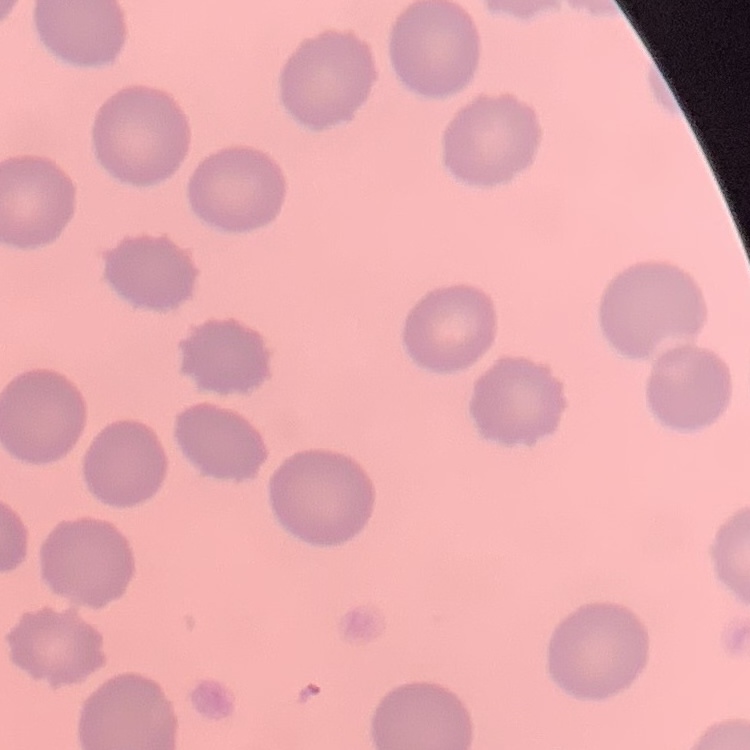
The erythrocytes show no rouleaux formation. Thin peripheral smear. Field's or Giemsa stain. Square crop of a larger photomicrograph.